Identify the parasite.
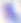
Toxoplasma gondii.

Summary:
  - Modality: photomicrograph
  - Magnification: 400x